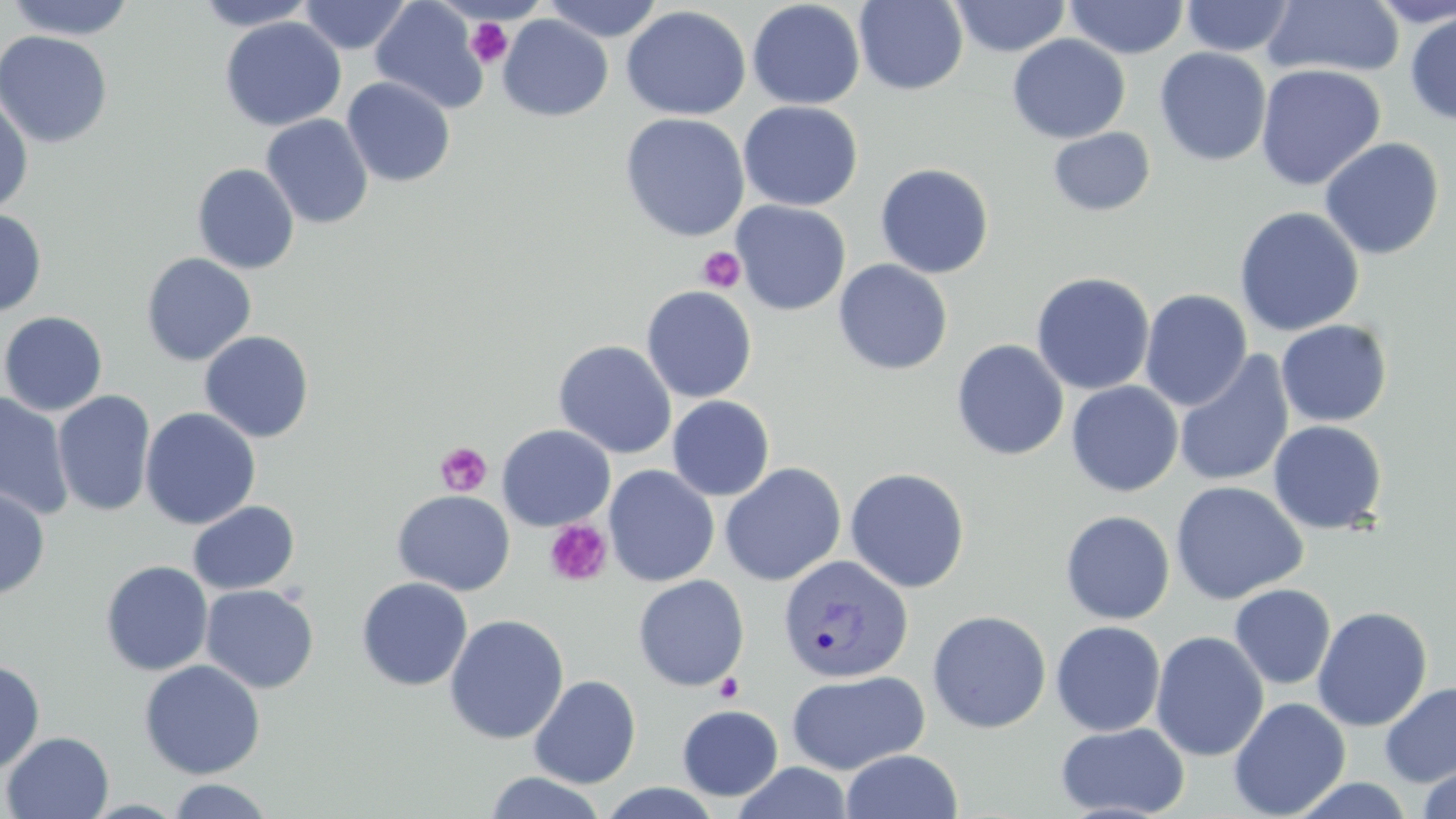

slide-level diagnosis = Plasmodium vivax
platelet locations = approximate bounding boxes as [x1, y1, x2, y2] in pixels: [466, 17, 514, 68], [697, 246, 746, 293], [435, 442, 492, 496], [543, 519, 613, 588], [714, 673, 745, 703]
image size = 1456×819 pixels
magnification = 1000x
uninfected red blood cell locations = approximate bounding boxes as [x1, y1, x2, y2] in pixels: [4, 0, 136, 41], [191, 0, 319, 31], [298, 0, 413, 55], [370, 0, 489, 115], [541, 0, 665, 42], [949, 0, 1071, 57], [1180, 0, 1296, 57], [1365, 0, 1456, 27], [747, 1, 866, 110], [854, 1, 969, 95], [1064, 1, 1189, 59], [1261, 1, 1405, 80], [621, 5, 751, 121], [1404, 10, 1456, 125], [498, 14, 613, 121], [220, 17, 346, 131], [0, 29, 113, 149], [1006, 34, 1131, 143], [1154, 47, 1272, 166], [1255, 63, 1386, 191], [341, 77, 456, 188], [0, 90, 34, 217], [738, 101, 863, 211], [619, 112, 750, 243], [260, 114, 373, 229], [1047, 127, 1156, 216], [1319, 137, 1445, 261], [192, 163, 299, 275], [875, 163, 994, 279], [731, 200, 851, 316], [1233, 206, 1365, 337], [0, 208, 48, 317], [140, 253, 257, 366], [833, 259, 953, 375], [1030, 271, 1155, 396], [641, 285, 758, 403], [1139, 289, 1253, 411], [0, 311, 108, 416], [1276, 319, 1393, 427], [199, 330, 315, 443], [951, 339, 1069, 462], [553, 340, 677, 459], [1172, 352, 1294, 489], [1065, 381, 1183, 497], [52, 390, 156, 517], [0, 391, 74, 521], [667, 395, 775, 501], [139, 407, 261, 530], [1267, 420, 1388, 535], [496, 424, 616, 531], [719, 462, 846, 587], [623, 464, 731, 690], [604, 465, 720, 587], [845, 467, 970, 593], [1170, 480, 1308, 605], [0, 485, 50, 600], [392, 489, 515, 596], [187, 500, 300, 595], [1060, 510, 1175, 625], [100, 560, 213, 676], [632, 574, 749, 691], [356, 577, 473, 691], [200, 584, 319, 693], [1228, 584, 1336, 690], [1312, 605, 1433, 731], [927, 609, 1052, 734], [444, 614, 569, 744], [1050, 620, 1166, 736], [1150, 631, 1269, 762], [139, 659, 265, 780], [0, 660, 45, 775], [786, 669, 929, 775], [528, 675, 641, 789], [1379, 681, 1456, 787], [1228, 697, 1351, 818], [677, 704, 783, 801], [1055, 722, 1190, 818], [2, 731, 114, 818], [840, 749, 963, 819], [732, 762, 853, 819], [1417, 765, 1456, 819], [484, 771, 608, 819], [1288, 775, 1416, 818], [166, 778, 275, 818], [592, 781, 726, 818]
Plasmodium vivax-infected red blood cell locations = approximate bounding boxes as [x1, y1, x2, y2] in pixels: [777, 553, 914, 683]
preparation = thin blood smear
modality = light microscopy
stain = May-Grünwald-Giemsa
field of view = single